Point out every Plasmodium parasite.
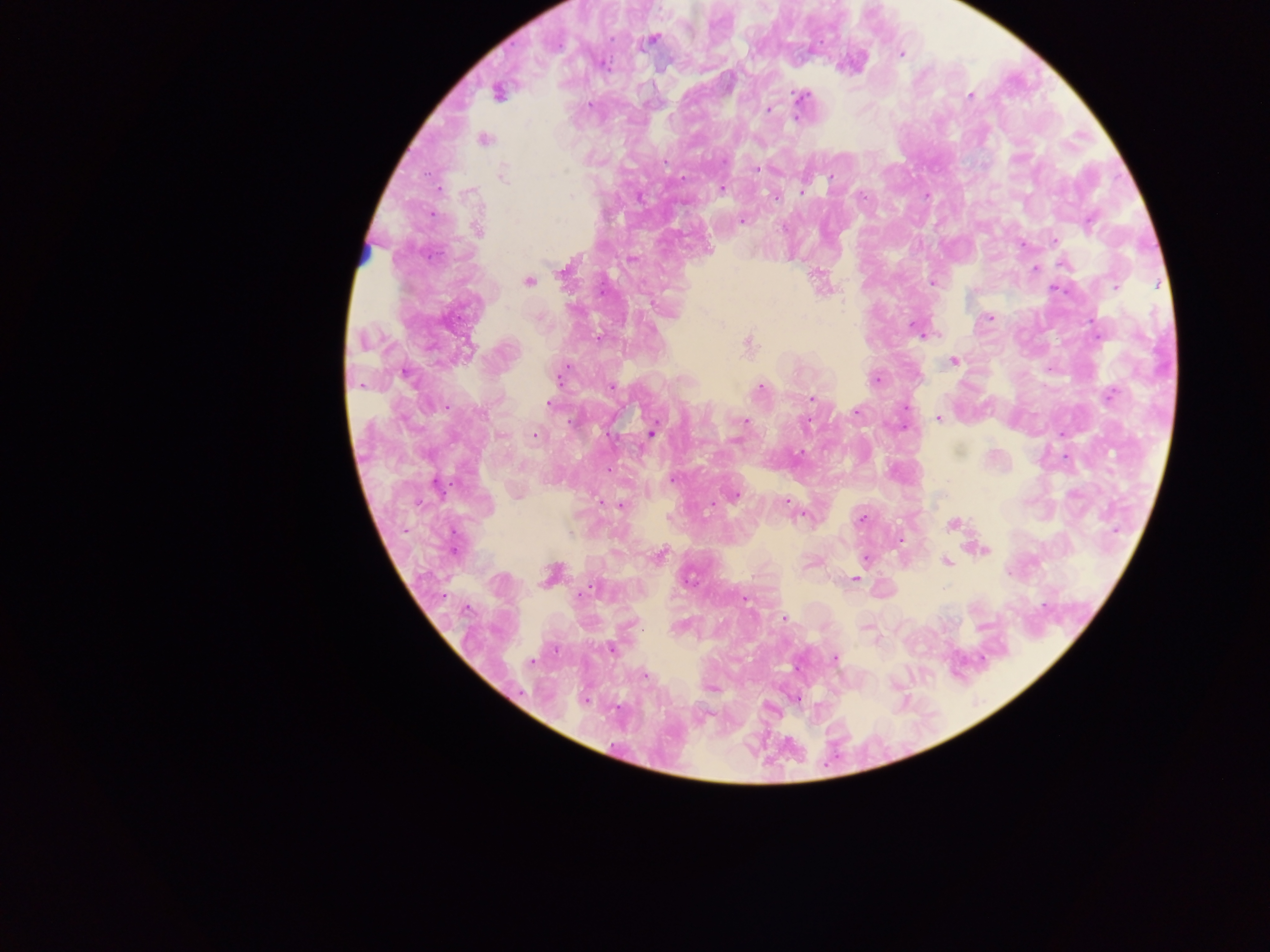

Approximate centers as x y in pixels.
Plasmodium parasites: 650 39; 900 53; 602 63; 497 92; 971 95; 801 97; 768 108; 483 139; 756 170; 503 174; 830 178; 721 188; 801 192; 926 195; 741 220; 477 229; 1053 240; 1021 244; 706 249; 631 258; 1035 267; 815 272; 528 281; 932 282; 1116 287; 988 317; 916 328; 599 338; 748 344; 954 360; 405 372; 560 375; 876 379; 760 387; 1110 395; 812 398; 549 403; 905 407; 855 412; 939 418; 743 421; 806 421; 652 431; 1061 433; 535 435; 608 470; 673 479; 733 496; 621 505; 804 514; 860 518; 952 525; 983 549; 658 556; 865 557; 946 561; 551 573; 854 579; 743 598; 784 619; 866 627; 611 648; 836 658; 797 669; 644 676; 711 688; 795 698; 584 699.

Summary:
  - Field of view: single
  - Preparation: thick blood smear
  - Capture: mobile-phone photograph through a microscope
  - Country: Ghana
  - Image size: 1270×952 pixels